Report the malaria status of this cell.
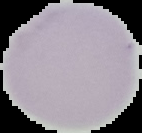
It is uninfected.

image size = 142×133 pixels
preparation = thin blood smear
image type = segmented cell region on a black background